Name the blood parasite species.
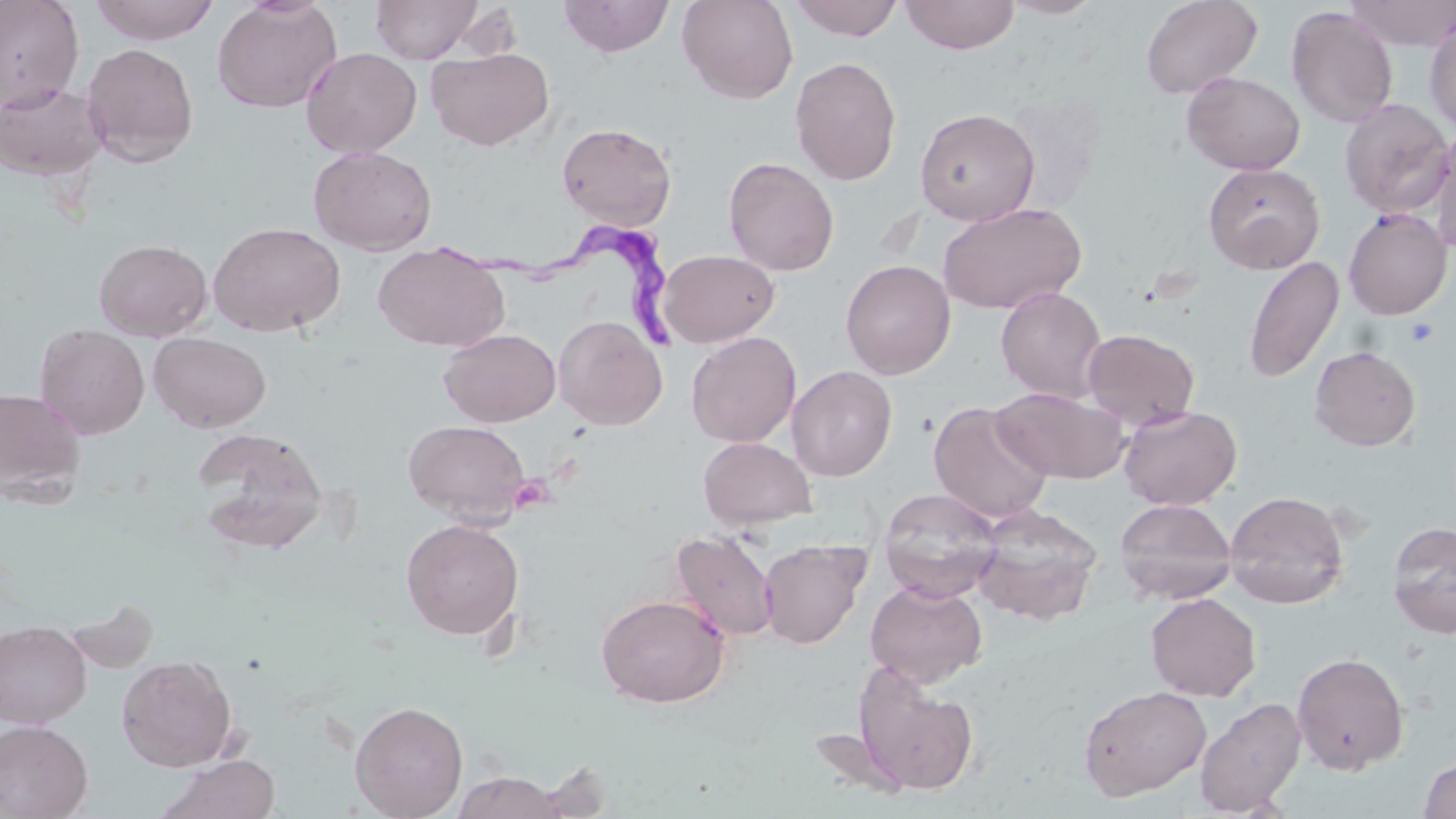

Trypanosoma brucei.

Summary:
  - Coordinate format: approximate bounding boxes as named x1/y1/x2/y2 corners in pixels
  - Uninfected red blood cell locations: (x1=0, y1=0, x2=85, y2=112), (x1=91, y1=0, x2=221, y2=45), (x1=212, y1=0, x2=342, y2=114), (x1=370, y1=0, x2=483, y2=63), (x1=558, y1=0, x2=676, y2=58), (x1=677, y1=0, x2=799, y2=103), (x1=788, y1=0, x2=905, y2=41), (x1=900, y1=0, x2=1020, y2=54), (x1=999, y1=0, x2=1107, y2=19), (x1=1140, y1=0, x2=1262, y2=98), (x1=1344, y1=0, x2=1456, y2=50), (x1=1285, y1=6, x2=1398, y2=128), (x1=1425, y1=15, x2=1456, y2=134), (x1=81, y1=42, x2=200, y2=167), (x1=301, y1=47, x2=422, y2=158), (x1=426, y1=48, x2=554, y2=151), (x1=789, y1=56, x2=902, y2=185), (x1=1181, y1=71, x2=1306, y2=175), (x1=0, y1=81, x2=106, y2=181), (x1=1338, y1=98, x2=1454, y2=217), (x1=915, y1=108, x2=1040, y2=226), (x1=556, y1=121, x2=677, y2=230), (x1=1427, y1=126, x2=1456, y2=252), (x1=308, y1=145, x2=437, y2=255), (x1=723, y1=157, x2=839, y2=276), (x1=1203, y1=162, x2=1325, y2=274), (x1=937, y1=201, x2=1087, y2=315), (x1=1343, y1=208, x2=1452, y2=320), (x1=208, y1=221, x2=345, y2=337), (x1=93, y1=239, x2=212, y2=341), (x1=372, y1=241, x2=509, y2=352), (x1=657, y1=249, x2=779, y2=347), (x1=1243, y1=256, x2=1345, y2=384), (x1=840, y1=259, x2=956, y2=379), (x1=995, y1=286, x2=1108, y2=403), (x1=553, y1=315, x2=667, y2=430), (x1=35, y1=324, x2=150, y2=439), (x1=439, y1=328, x2=561, y2=426), (x1=1083, y1=328, x2=1200, y2=430), (x1=686, y1=331, x2=801, y2=447), (x1=149, y1=333, x2=271, y2=432), (x1=1309, y1=345, x2=1421, y2=451), (x1=787, y1=365, x2=897, y2=481), (x1=0, y1=386, x2=87, y2=502), (x1=991, y1=387, x2=1128, y2=483), (x1=929, y1=400, x2=1054, y2=525), (x1=1118, y1=404, x2=1242, y2=510), (x1=404, y1=419, x2=531, y2=525), (x1=193, y1=427, x2=329, y2=554), (x1=698, y1=437, x2=816, y2=529), (x1=878, y1=487, x2=1003, y2=602), (x1=1224, y1=490, x2=1349, y2=609), (x1=1114, y1=498, x2=1236, y2=604), (x1=972, y1=504, x2=1103, y2=626), (x1=400, y1=518, x2=524, y2=640), (x1=1387, y1=521, x2=1456, y2=639), (x1=668, y1=530, x2=780, y2=642), (x1=759, y1=539, x2=868, y2=649), (x1=865, y1=579, x2=987, y2=687), (x1=1145, y1=592, x2=1262, y2=701), (x1=595, y1=593, x2=730, y2=707), (x1=0, y1=620, x2=92, y2=728), (x1=1291, y1=651, x2=1410, y2=775), (x1=116, y1=654, x2=237, y2=771), (x1=852, y1=662, x2=980, y2=797), (x1=1078, y1=685, x2=1212, y2=800), (x1=1195, y1=697, x2=1305, y2=816), (x1=349, y1=700, x2=468, y2=819), (x1=0, y1=719, x2=93, y2=819), (x1=157, y1=754, x2=281, y2=819), (x1=1418, y1=756, x2=1456, y2=818), (x1=452, y1=771, x2=566, y2=818)
  - Platelet locations: (x1=1404, y1=317, x2=1439, y2=347)
  - Trypanosoma brucei locations: (x1=442, y1=230, x2=694, y2=348)
  - Preparation: thin blood smear
  - Image size: 1456×819 pixels
  - Stain: May-Grünwald-Giemsa
  - Modality: optical microscopy
  - Field of view: single
  - Magnification: 1000x